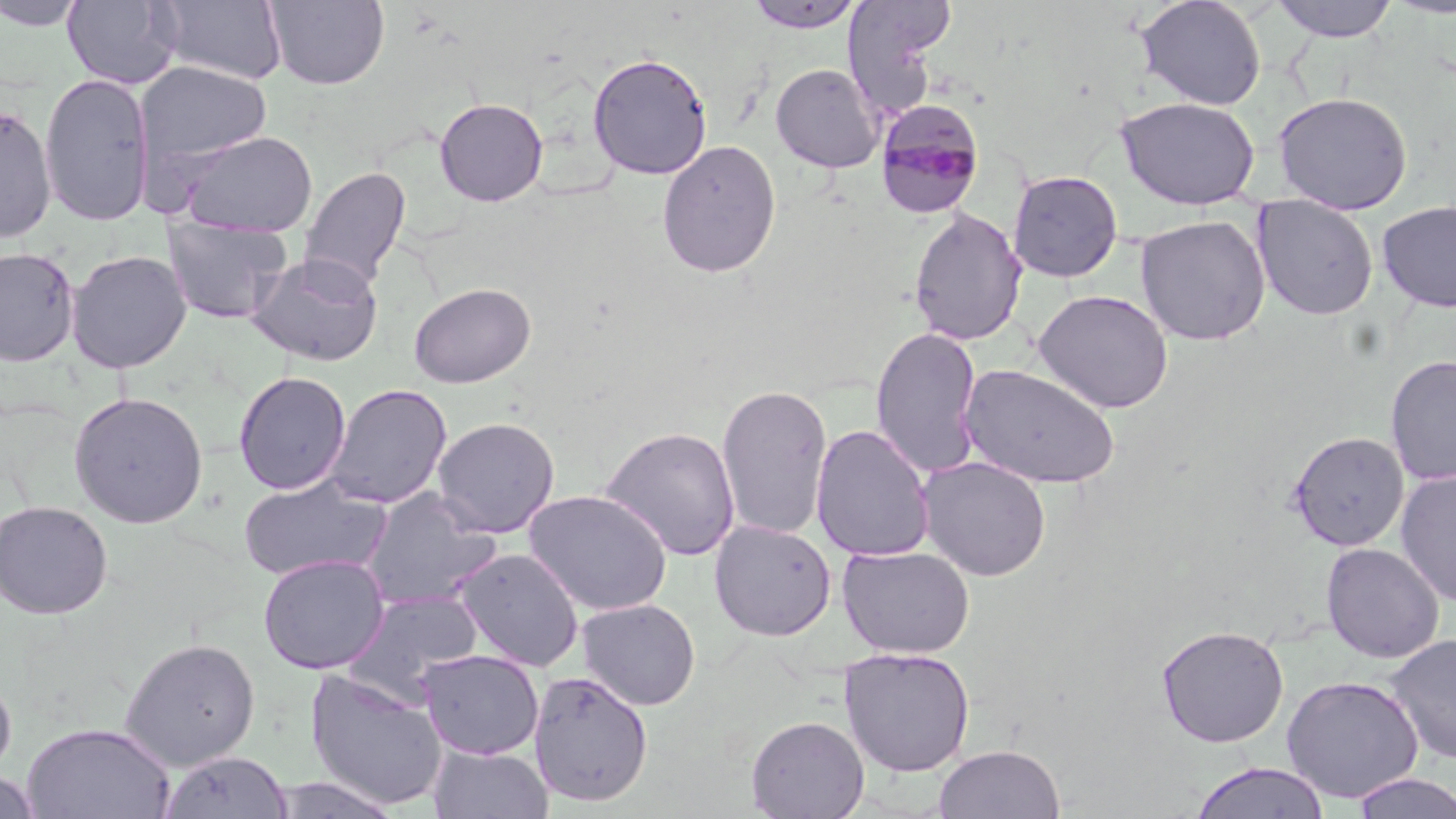

slide-level diagnosis = Plasmodium malariae
image size = 1456×819 pixels
magnification = 1000x
modality = light microscopy
stain = May-Grünwald-Giemsa
Plasmodium malariae-infected red blood cell locations = approximate bounding boxes as named x1/y1/x2/y2 corners in pixels: (x1=874, y1=100, x2=986, y2=219)
preparation = thin blood smear
field of view = one of a larger specimen
uninfected red blood cell locations = approximate bounding boxes as named x1/y1/x2/y2 corners in pixels: (x1=63, y1=0, x2=181, y2=89), (x1=1135, y1=0, x2=1267, y2=111), (x1=1268, y1=0, x2=1400, y2=42), (x1=0, y1=1, x2=89, y2=31), (x1=156, y1=1, x2=288, y2=85), (x1=265, y1=1, x2=389, y2=89), (x1=745, y1=1, x2=866, y2=33), (x1=842, y1=1, x2=953, y2=114), (x1=587, y1=52, x2=713, y2=179), (x1=136, y1=62, x2=272, y2=169), (x1=770, y1=63, x2=884, y2=173), (x1=39, y1=73, x2=155, y2=226), (x1=1273, y1=92, x2=1413, y2=214), (x1=1115, y1=96, x2=1260, y2=209), (x1=434, y1=97, x2=548, y2=207), (x1=0, y1=104, x2=57, y2=243), (x1=179, y1=130, x2=318, y2=237), (x1=657, y1=139, x2=781, y2=279), (x1=300, y1=166, x2=411, y2=291), (x1=1008, y1=170, x2=1123, y2=283), (x1=1252, y1=196, x2=1379, y2=321), (x1=1377, y1=200, x2=1456, y2=313), (x1=908, y1=207, x2=1027, y2=346), (x1=1135, y1=214, x2=1271, y2=347), (x1=163, y1=218, x2=293, y2=325), (x1=0, y1=246, x2=80, y2=367), (x1=65, y1=249, x2=192, y2=373), (x1=246, y1=251, x2=384, y2=366), (x1=409, y1=282, x2=536, y2=388), (x1=1033, y1=289, x2=1174, y2=414), (x1=870, y1=325, x2=983, y2=480), (x1=1384, y1=355, x2=1456, y2=486), (x1=959, y1=364, x2=1120, y2=490), (x1=233, y1=371, x2=351, y2=495), (x1=716, y1=382, x2=833, y2=541), (x1=325, y1=384, x2=452, y2=509), (x1=69, y1=391, x2=209, y2=529), (x1=431, y1=416, x2=560, y2=538), (x1=810, y1=424, x2=936, y2=562), (x1=600, y1=426, x2=740, y2=561), (x1=1288, y1=430, x2=1409, y2=550), (x1=918, y1=457, x2=1051, y2=581), (x1=1395, y1=469, x2=1456, y2=607), (x1=237, y1=476, x2=392, y2=582), (x1=361, y1=488, x2=501, y2=610), (x1=523, y1=489, x2=673, y2=616), (x1=0, y1=499, x2=113, y2=619), (x1=709, y1=519, x2=837, y2=641), (x1=1321, y1=542, x2=1445, y2=663), (x1=838, y1=545, x2=974, y2=658), (x1=452, y1=547, x2=584, y2=671), (x1=257, y1=553, x2=390, y2=674), (x1=342, y1=590, x2=486, y2=702), (x1=577, y1=598, x2=701, y2=711), (x1=1155, y1=624, x2=1289, y2=747), (x1=1385, y1=634, x2=1456, y2=764), (x1=119, y1=637, x2=261, y2=771), (x1=840, y1=647, x2=975, y2=778), (x1=418, y1=649, x2=544, y2=760), (x1=304, y1=669, x2=449, y2=811), (x1=529, y1=670, x2=654, y2=807), (x1=0, y1=672, x2=16, y2=782), (x1=1281, y1=675, x2=1424, y2=802), (x1=745, y1=715, x2=869, y2=818), (x1=21, y1=721, x2=176, y2=819), (x1=428, y1=744, x2=554, y2=818), (x1=932, y1=744, x2=1066, y2=818), (x1=158, y1=749, x2=291, y2=819), (x1=1188, y1=762, x2=1332, y2=819), (x1=1, y1=770, x2=41, y2=819), (x1=1349, y1=772, x2=1456, y2=818), (x1=271, y1=776, x2=402, y2=818)